Identify the parasite.
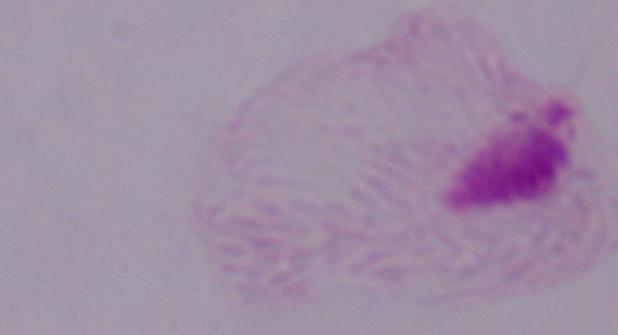

This is a trichomonad.

1000x magnification. Photomicrograph.